Identify the cell.
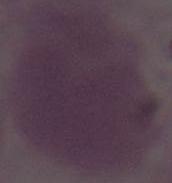

An erythrocyte.

magnification = 1000x
modality = micrograph